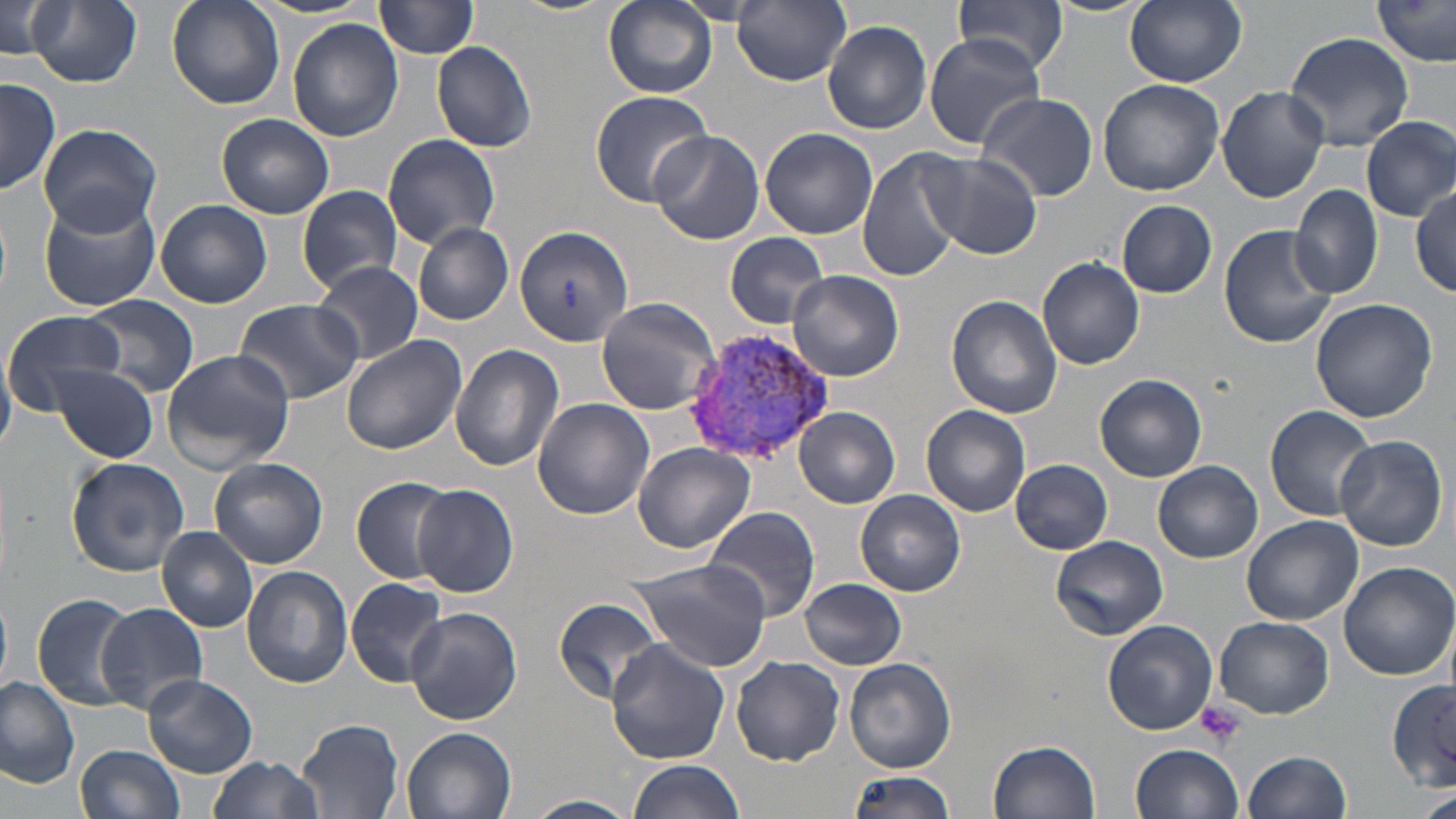

Approximate bounding boxes as [x1, y1, x2, y2] in pixels. Plasmodium vivax-infected red blood cell locations: [685, 326, 834, 463]. Uninfected red blood cell locations: [24, 0, 143, 87], [166, 0, 283, 109], [375, 0, 480, 58], [603, 0, 717, 98], [954, 0, 1070, 75], [1045, 0, 1153, 17], [1124, 0, 1247, 88], [1373, 0, 1456, 67], [672, 1, 770, 24], [734, 1, 851, 86], [2, 3, 66, 62], [288, 18, 403, 141], [823, 19, 933, 133], [1284, 31, 1415, 149], [922, 35, 1046, 145], [432, 40, 537, 153], [1, 76, 60, 195], [1096, 78, 1226, 196], [1216, 85, 1329, 204], [589, 90, 712, 206], [976, 92, 1097, 201], [217, 112, 334, 219], [1361, 116, 1456, 221], [38, 121, 163, 236], [759, 127, 879, 239], [648, 130, 765, 245], [382, 135, 500, 247], [856, 145, 968, 283], [921, 150, 1043, 259], [1288, 184, 1383, 300], [1411, 184, 1456, 296], [297, 185, 404, 292], [37, 192, 160, 312], [155, 199, 272, 309], [1117, 200, 1217, 299], [412, 221, 515, 325], [512, 224, 635, 348], [1218, 224, 1338, 349], [723, 232, 829, 327], [1037, 257, 1148, 370], [311, 260, 423, 365], [790, 270, 903, 381], [947, 295, 1064, 418], [82, 296, 201, 394], [596, 298, 722, 415], [1310, 298, 1438, 423], [232, 299, 365, 406], [4, 310, 122, 411], [340, 334, 467, 454], [450, 343, 564, 472], [0, 349, 16, 454], [160, 350, 295, 472], [52, 364, 159, 462], [1095, 374, 1207, 481], [532, 397, 655, 520], [922, 404, 1031, 516], [1264, 404, 1380, 522], [795, 407, 899, 506], [1335, 434, 1448, 550], [632, 442, 755, 552], [209, 457, 328, 569], [67, 458, 190, 576], [1010, 458, 1113, 555], [1153, 462, 1263, 563], [351, 476, 459, 583], [412, 484, 517, 598], [856, 490, 966, 597], [700, 507, 823, 622], [1241, 514, 1363, 625], [157, 526, 258, 633], [1050, 536, 1168, 640], [628, 554, 773, 674], [1338, 562, 1454, 681], [241, 567, 353, 688], [346, 577, 450, 688], [800, 579, 907, 669], [32, 592, 143, 713], [0, 593, 12, 690], [553, 597, 664, 703], [97, 603, 208, 714], [406, 607, 522, 725], [1215, 617, 1333, 719], [1103, 620, 1218, 734], [606, 639, 730, 763], [732, 656, 845, 765], [844, 656, 955, 773], [143, 672, 258, 778], [0, 676, 81, 786], [1387, 680, 1456, 786], [295, 718, 405, 819], [403, 727, 517, 819], [989, 739, 1102, 818], [1133, 743, 1244, 819], [78, 744, 185, 819], [1244, 749, 1352, 819], [208, 755, 324, 819], [627, 759, 747, 819], [843, 771, 957, 819], [1415, 790, 1456, 819], [523, 794, 638, 818]. Platelet locations: [1196, 700, 1246, 748]. Slide-level diagnosis: Plasmodium vivax. One field of a larger specimen. Image is 1456×819 pixels. Thin blood film. 1000x magnification. Optical microscopy. May-Grünwald-Giemsa-stained preparation.